Report the malaria status of this cell.
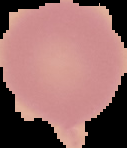
Uninfected.

Image is 127×148 pixels. From a thin blood smear. Segmented cell region on a black background.